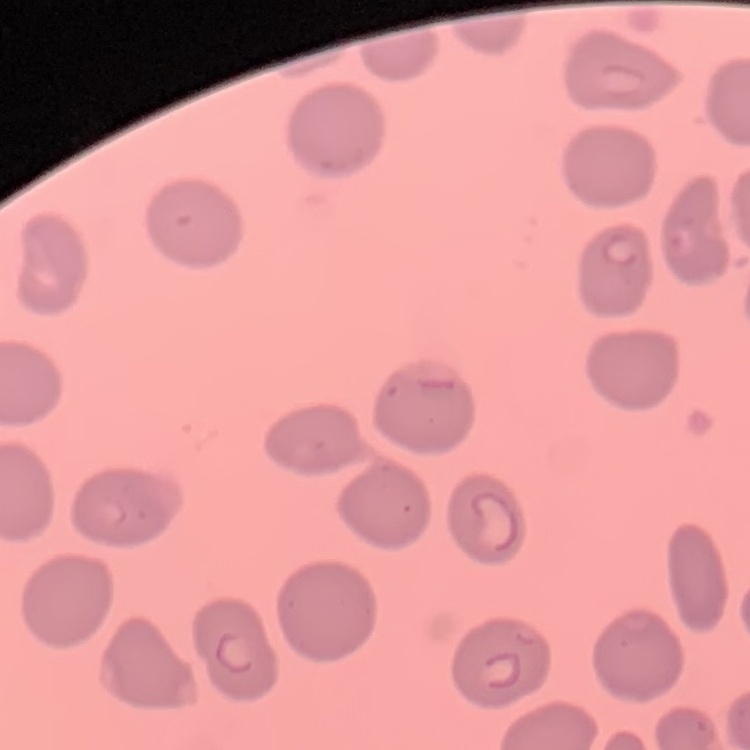

red blood cell morphology = no rouleaux formation
preparation = thin blood smear
image type = square crop of a larger photomicrograph
stain = Field's or Giemsa